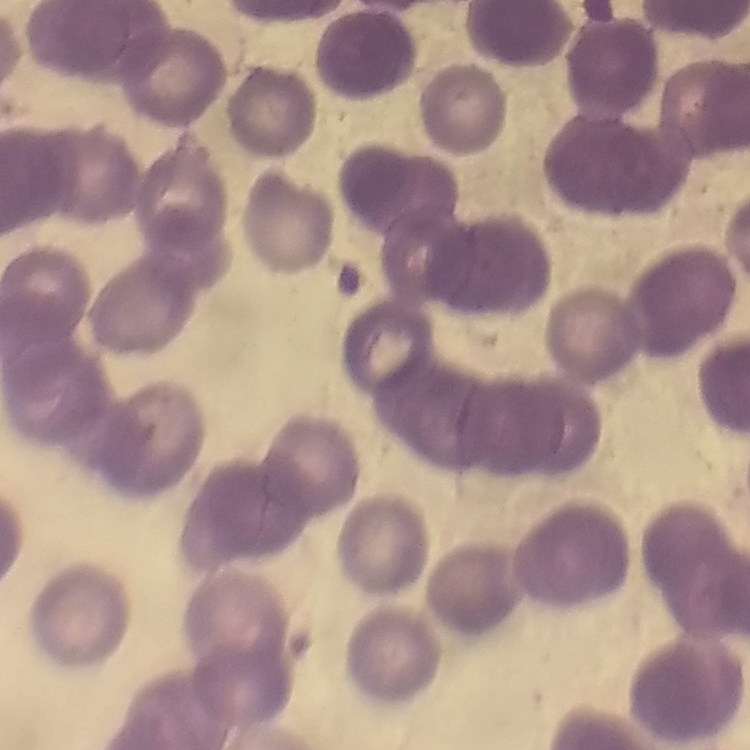
erythrocyte_morphology: rouleaux formation
preparation: thin blood smear
image_type: one tile cut from a larger photomicrograph
stain: Field's or Giemsa